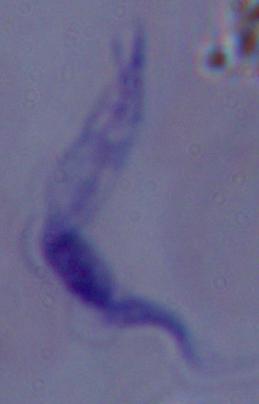

Summary:
  - Magnification: 1000x
  - Identification: trypanosome
  - Modality: micrograph